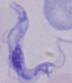

Summary:
  - Magnification: 1000x
  - Modality: photomicrograph
  - Identification: trypanosome